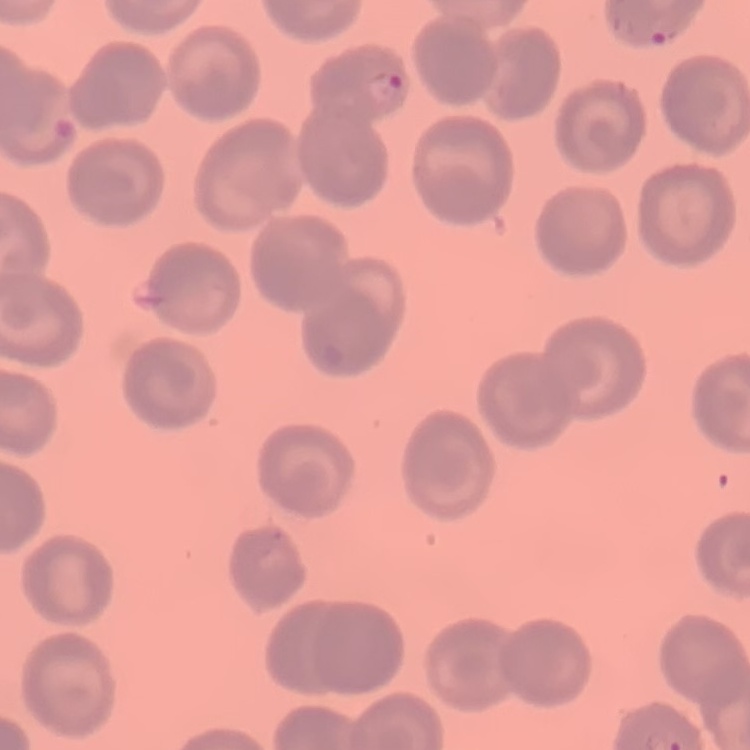

Summary:
  - Erythrocyte morphology: no rouleaux formation
  - Image type: one tile cut from a larger photomicrograph
  - Stain: Field's or Giemsa
  - Preparation: thin peripheral smear